Give a bounding box for every parasitised red blood cell.
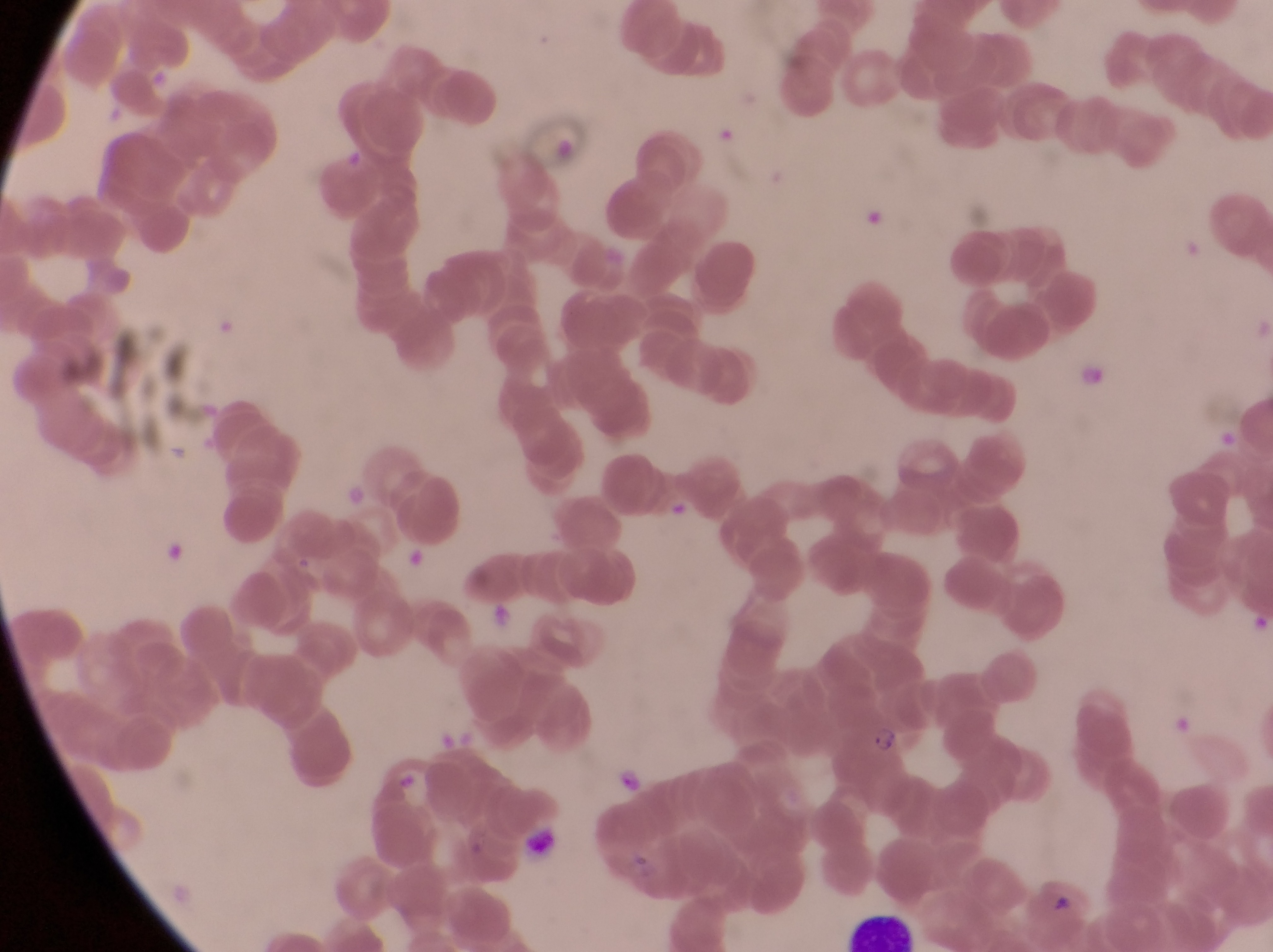

Approximate bounding boxes as left top right bottom in pixels.
Parasitised red blood cells: 833 714 918 816.

Summary:
  - Artifact (platelet-like body, stain precipitate, or debris) locations: 490 601 516 629; 618 767 647 793
  - Leukocyte locations: 517 828 565 860; 846 908 919 951
  - Field of view: single
  - Image size: 1273×952 pixels
  - Country: Uganda
  - Preparation: thin blood smear
  - Capture: smartphone photograph through the eyepiece of an Olympus CX-23 microscope
  - Magnification: 1000x